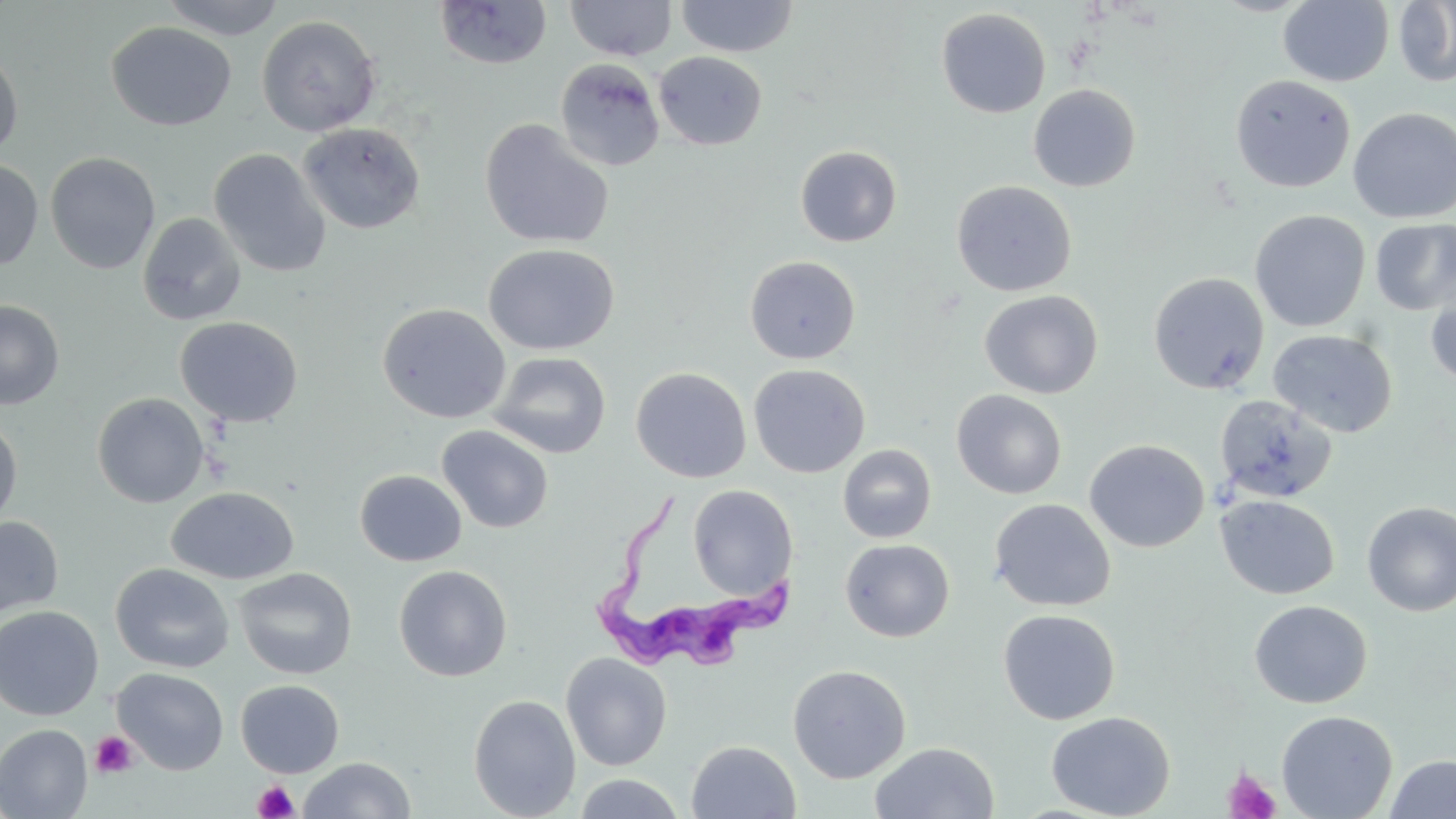

slide-level diagnosis = Trypanosoma brucei
field of view = single
stain = May-Grünwald-Giemsa
uninfected red blood cell locations = approximate bounding boxes as (x1,y1)-(x2,y2) corner pairs in pixels: (159,0)-(287,40), (676,0)-(798,58), (1394,0)-(1456,87), (434,1)-(552,70), (565,1)-(677,61), (1278,1)-(1394,87), (936,8)-(1051,118), (256,15)-(382,137), (106,22)-(236,131), (0,44)-(24,159), (653,51)-(767,151), (555,58)-(665,171), (1230,74)-(1356,193), (1028,83)-(1141,192), (1348,107)-(1456,224), (479,119)-(615,249), (297,122)-(426,235), (795,145)-(902,247), (209,148)-(331,278), (45,152)-(161,273), (0,159)-(43,271), (951,180)-(1077,297), (1249,209)-(1370,332), (137,212)-(247,326), (1370,218)-(1456,317), (483,243)-(619,355), (744,255)-(861,364), (1148,272)-(1269,394), (1426,287)-(1456,389), (979,290)-(1103,399), (0,300)-(65,410), (376,302)-(511,424), (175,316)-(303,428), (1266,328)-(1397,438), (488,351)-(611,458), (748,363)-(870,478), (631,367)-(751,483), (951,390)-(1067,499), (92,392)-(210,508), (1215,394)-(1338,504), (0,417)-(23,529), (436,424)-(554,533), (1084,439)-(1209,553), (838,444)-(936,543), (354,470)-(467,567), (688,485)-(798,599), (166,487)-(299,585), (1216,495)-(1340,600), (989,498)-(1115,612), (1361,501)-(1456,616), (0,516)-(64,620), (840,538)-(955,642), (111,563)-(235,673), (394,564)-(512,681), (233,567)-(358,680), (1249,600)-(1372,709), (0,605)-(104,720), (998,608)-(1120,725), (561,652)-(672,771), (787,664)-(911,783), (112,668)-(229,775), (235,679)-(344,778), (468,694)-(581,819), (1275,710)-(1398,819), (1046,711)-(1175,819), (0,724)-(93,819), (687,740)-(801,819), (870,742)-(999,819), (1384,755)-(1456,818), (298,757)-(415,818), (573,774)-(687,818)
magnification = 1000x
image size = 1456×819 pixels
preparation = thin blood film
platelet locations = approximate bounding boxes as (x1,y1)-(x2,y2) corner pairs in pixels: (90,731)-(138,779), (1222,766)-(1282,819), (253,780)-(299,819)
modality = optical microscopy
Trypanosoma brucei locations = approximate bounding boxes as (x1,y1)-(x2,y2) corner pairs in pixels: (589,493)-(802,680)